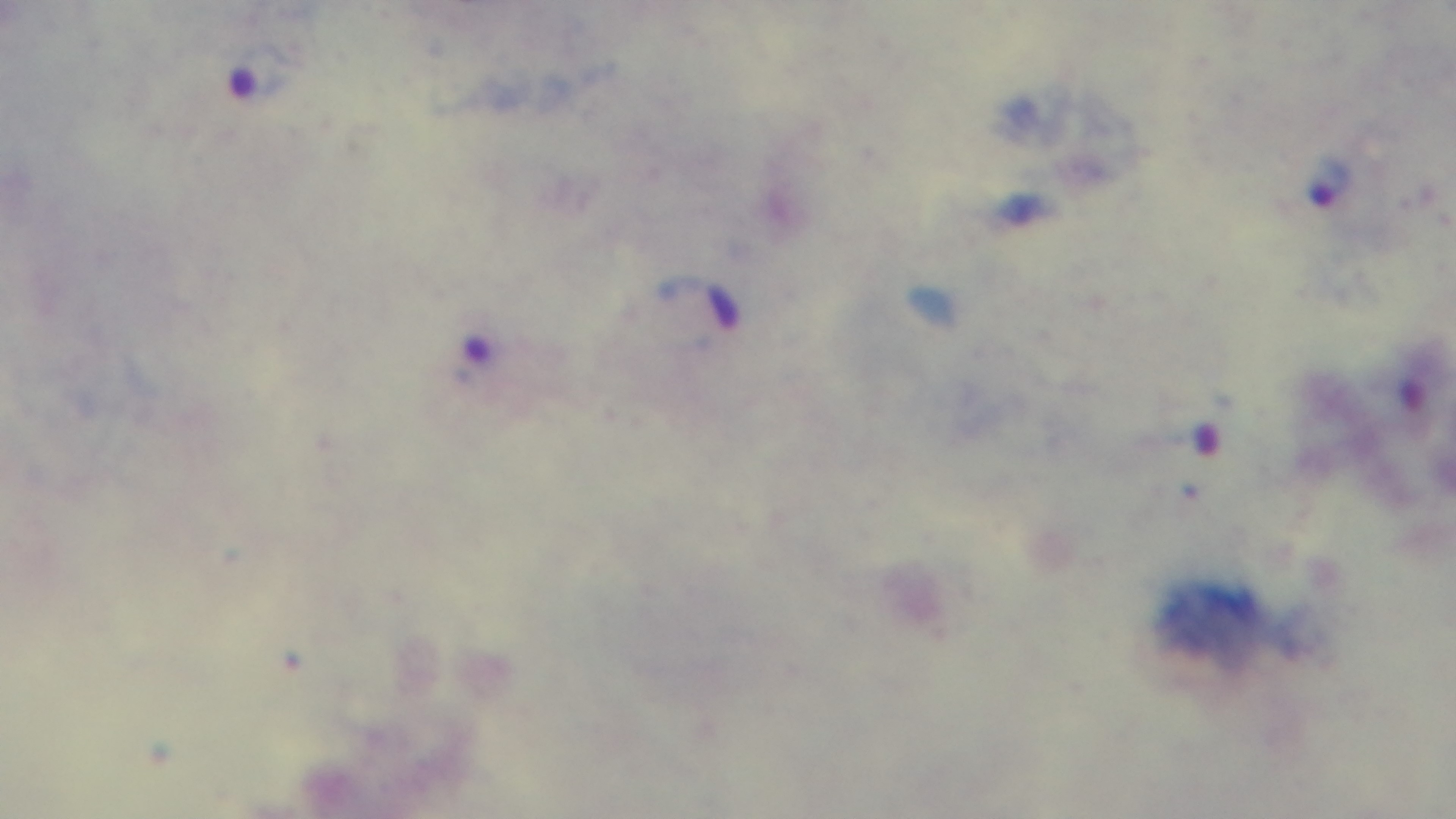

Summary:
  - Capture: mounted 4K digital camera
  - Preparation: thick blood film
  - Stain: Giemsa
  - Objective: 100x oil immersion
  - Modality: light microscopy
  - Malaria status: infected
  - Field of view: one from the slide